State which parasite is depicted.
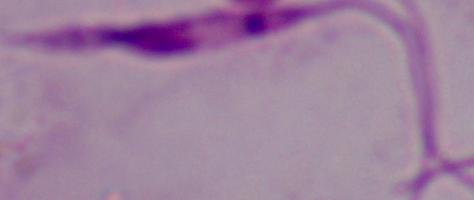
Leishmania.

modality = photomicrograph
magnification = 1000x